Describe the morphology of the red blood cells.
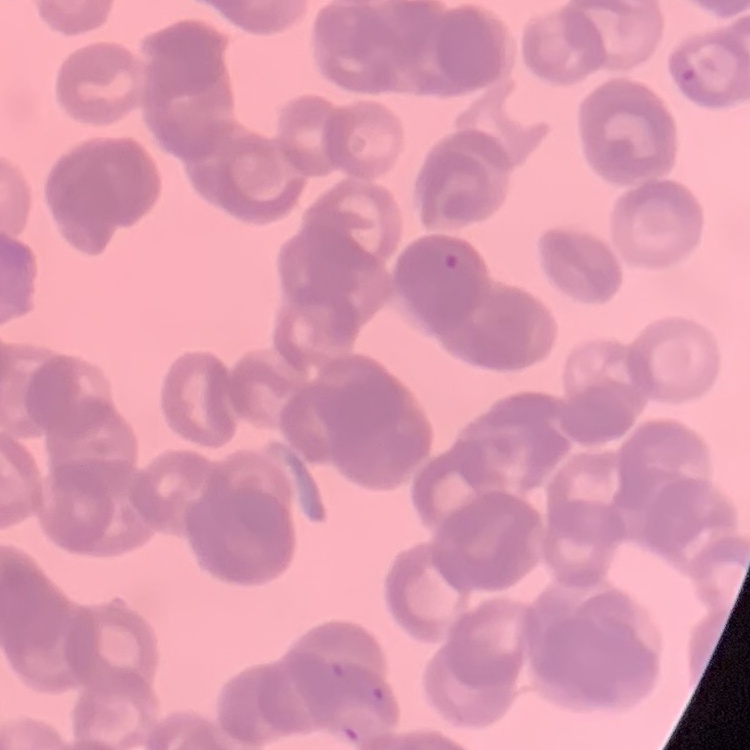
Rouleaux formation.

Thin blood film. One tile cut from a larger photomicrograph. Field's or Giemsa stain.